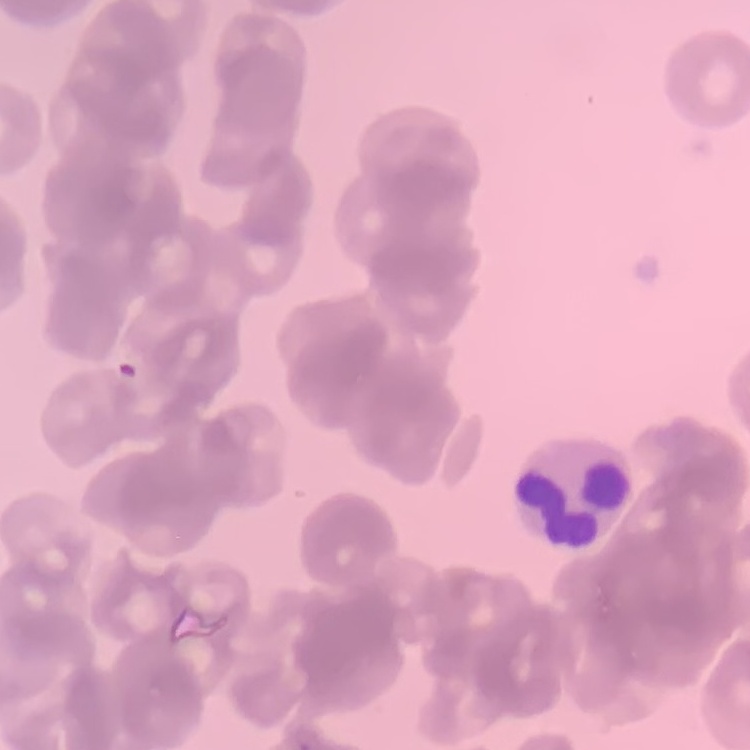

Summary:
  - Erythrocyte morphology: rouleaux formation
  - Stain: Field's or Giemsa
  - Image type: one tile cut from a larger photomicrograph
  - Preparation: thin blood smear